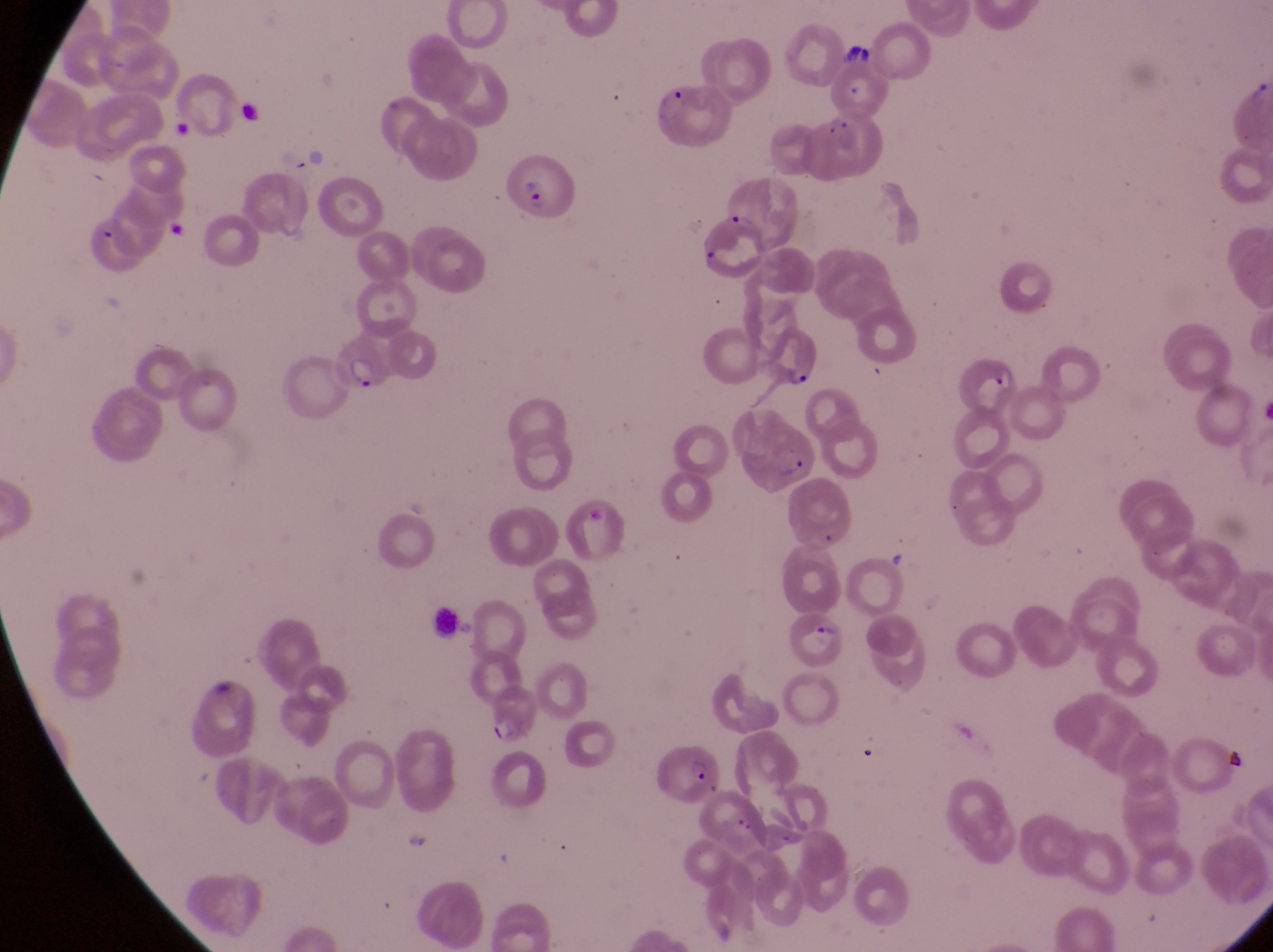
Approximate bounding boxes as left top right bottom in pixels. Parasitised red blood cell locations: 811 115 882 182; 507 157 582 219; 689 210 764 278; 762 325 819 388; 325 340 388 395; 959 345 1019 415; 746 427 820 492; 791 612 856 677; 482 691 545 744; 654 746 724 809. Captured by a smartphone held over the eyepiece of an Olympus CX-23 microscope. At a magnification of 1000x. Collected in Uganda. Image is 1273×952 pixels. Thin blood film. One field of view.